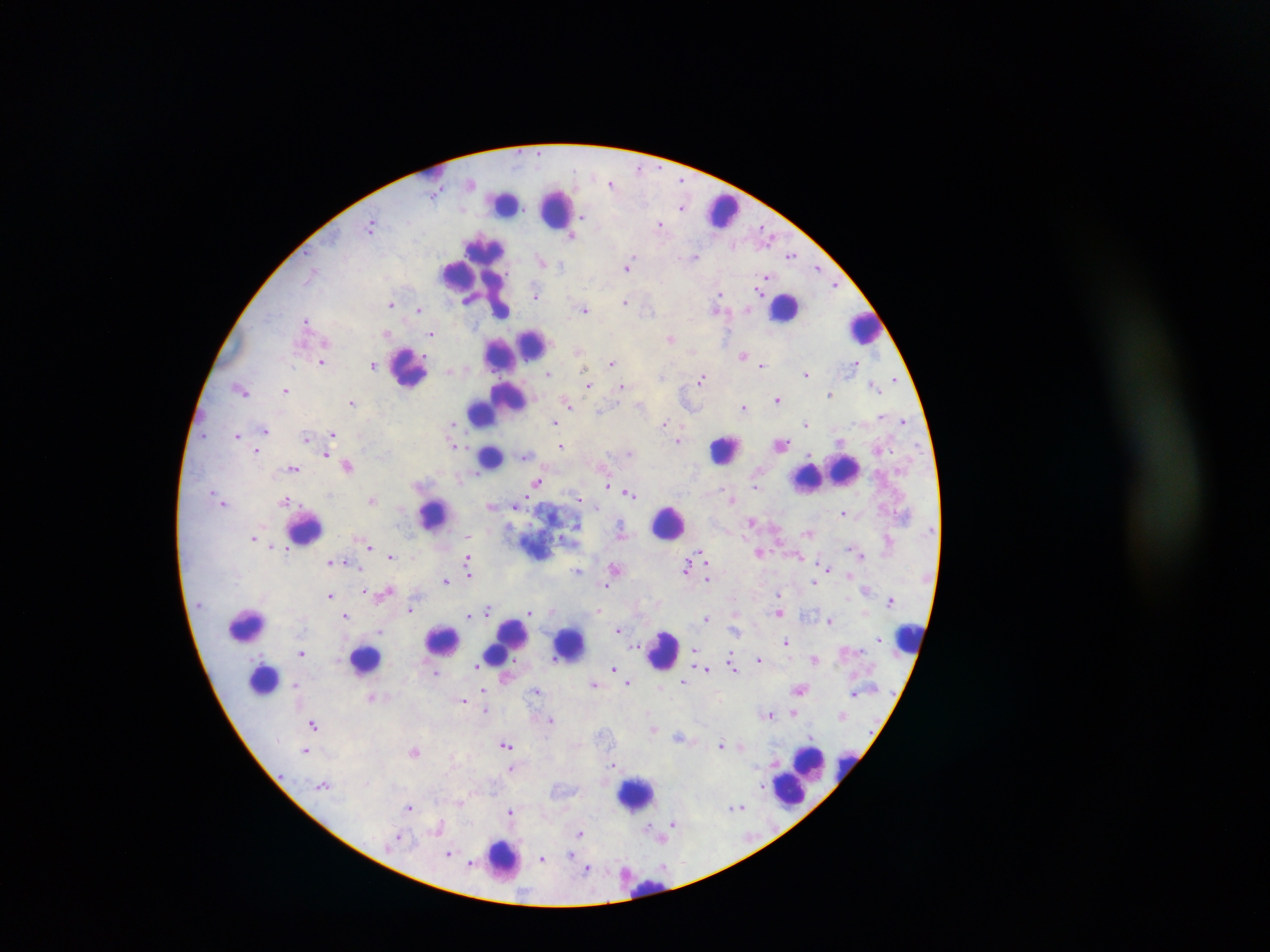
Approximate centers as x y in pixels. Leukocyte locations: 435 172; 506 202; 557 208; 721 210; 482 257; 457 272; 467 274; 783 307; 488 309; 865 328; 533 344; 515 349; 500 352; 409 367; 505 400; 481 411; 491 417; 726 449; 490 455; 829 473; 434 514; 668 522; 306 527; 247 625; 909 638; 443 640; 506 641; 569 643; 663 649; 366 659; 264 679; 808 762; 848 767; 799 777; 790 790; 637 794; 503 858; 644 883. Plasmodium parasite locations: 639 169; 682 179; 611 184; 681 207; 660 224; 372 225; 573 236; 791 254; 694 256; 541 260; 628 266; 818 267; 767 276; 836 284; 761 286; 536 295; 720 295; 625 302; 392 304; 419 309; 586 309; 720 309; 307 321; 387 333; 431 334; 671 337; 578 351; 692 352; 744 355; 322 361; 612 362; 856 362; 373 365; 762 366; 548 373; 806 374; 662 375; 894 378; 702 379; 588 385; 873 385; 622 386; 241 388; 286 389; 830 393; 778 400; 353 401; 568 403; 744 406; 600 409; 882 416; 904 421; 554 423; 665 423; 454 424; 806 424; 266 430; 333 433; 238 435; 307 437; 679 439; 840 441; 456 444; 782 444; 561 446; 257 450; 327 454; 526 456; 348 465; 293 468; 538 481; 608 486; 756 486; 629 492; 580 498; 733 498; 372 500; 223 502; 287 502; 491 504; 516 505; 844 511; 750 520; 576 526; 621 530; 809 533; 467 536; 254 537; 561 538; 274 546; 369 546; 282 547; 286 551; 759 553; 800 554; 703 555; 391 556; 861 556; 468 558; 330 561; 343 561; 469 565; 687 566; 362 568; 616 568; 828 570; 578 571; 469 574; 850 575; 708 578; 447 580; 813 582; 607 584; 366 591; 386 593; 779 593; 331 595; 891 599; 411 609; 489 609; 553 609; 599 611; 530 612; 778 612; 346 615; 469 615; 707 618; 830 620; 619 629; 379 631; 735 633; 878 639; 787 641; 638 647; 694 648; 302 653; 815 657; 759 659; 731 660; 477 665; 733 666; 614 667; 707 669; 436 671; 616 672; 685 681; 629 682; 593 683; 297 685; 661 686; 483 689; 799 689; 537 691; 854 694; 372 697; 464 700; 485 710; 793 712; 768 713; 552 719; 314 725; 653 729; 679 737; 506 743; 721 744; 741 745; 306 750; 415 750; 613 764; 512 767; 323 785; 762 786; 460 803; 410 806; 740 807; 511 811; 673 822; 440 824; 581 833; 400 835; 662 836; 449 852; 571 854; 543 859; 471 864; 587 868. Thick blood smear. Mobile-phone photograph taken through the microscope. Collected in Ghana. One field of view. Image is 1270×952 pixels.